Find each white blood cell.
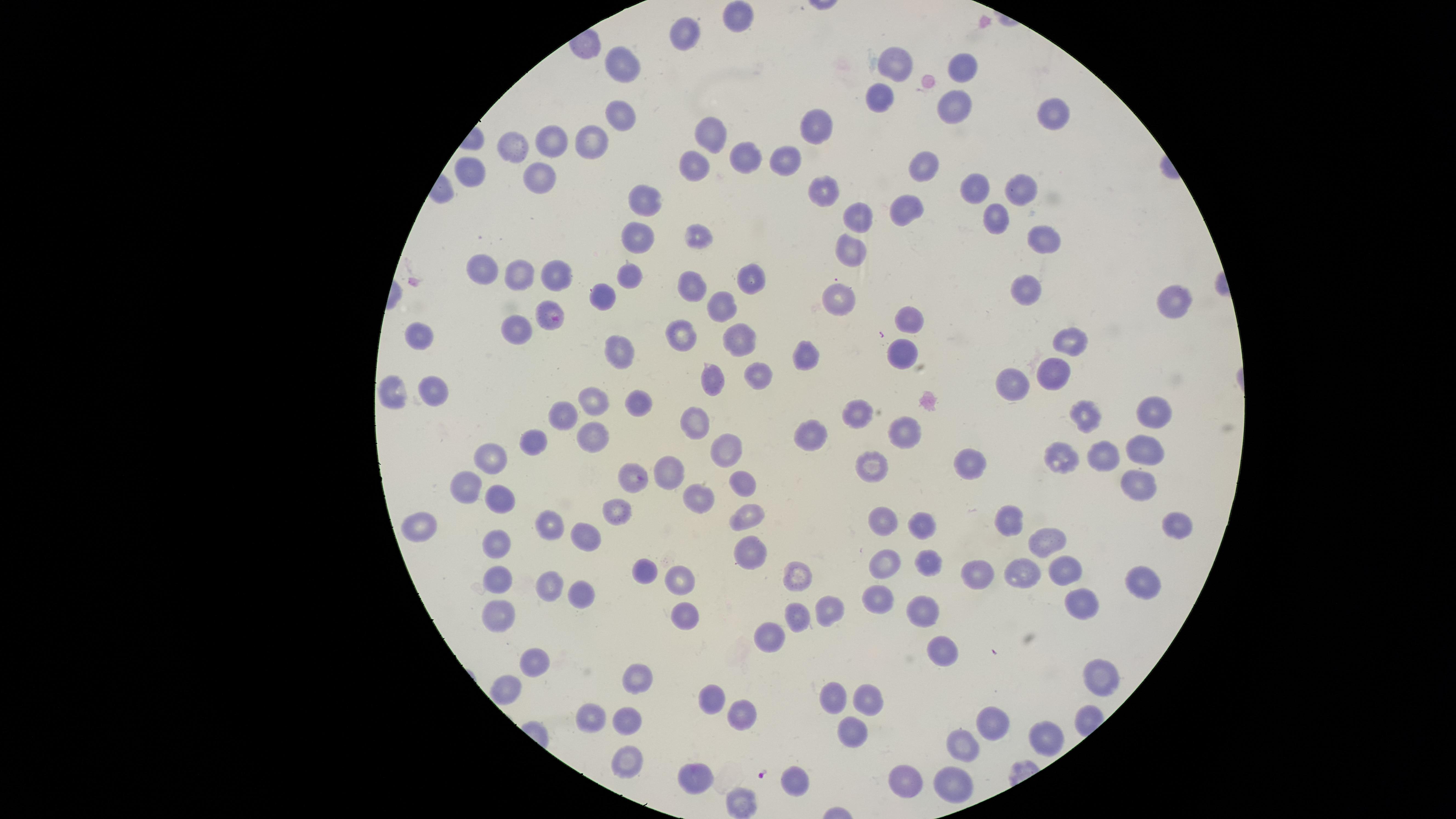

No white blood cells identified.

uninfected red blood cells = approximate marker points, in pixels from the top-left corner: (x=734, y=16), (x=688, y=31), (x=895, y=62), (x=622, y=63), (x=964, y=65), (x=880, y=95), (x=956, y=104), (x=1057, y=109), (x=620, y=119), (x=820, y=122), (x=709, y=127), (x=552, y=137), (x=591, y=139), (x=514, y=144), (x=743, y=158), (x=787, y=158), (x=924, y=165), (x=696, y=167), (x=540, y=174), (x=472, y=176), (x=1018, y=186), (x=820, y=187), (x=973, y=189), (x=644, y=201), (x=905, y=209), (x=858, y=212), (x=994, y=215), (x=696, y=233), (x=1039, y=233), (x=636, y=239), (x=850, y=245), (x=484, y=269), (x=517, y=272), (x=555, y=275), (x=628, y=275), (x=751, y=279), (x=691, y=288), (x=1025, y=290), (x=603, y=297), (x=840, y=299), (x=1179, y=300), (x=722, y=303), (x=910, y=317), (x=514, y=330), (x=680, y=333), (x=420, y=337), (x=1071, y=337), (x=737, y=339), (x=619, y=351), (x=904, y=351), (x=809, y=354), (x=1051, y=371), (x=757, y=372), (x=715, y=379), (x=1011, y=384), (x=395, y=389), (x=435, y=391), (x=635, y=399), (x=591, y=401), (x=1153, y=410), (x=863, y=412), (x=1081, y=412), (x=566, y=413), (x=695, y=423), (x=816, y=430), (x=910, y=431), (x=595, y=433), (x=727, y=443), (x=1144, y=443), (x=532, y=444), (x=1103, y=454), (x=496, y=455), (x=1063, y=457), (x=969, y=461), (x=874, y=464), (x=670, y=465), (x=628, y=476), (x=744, y=482), (x=1140, y=482), (x=474, y=486), (x=702, y=495), (x=501, y=498), (x=614, y=512), (x=750, y=512), (x=1007, y=519), (x=881, y=522), (x=1176, y=523), (x=418, y=525), (x=550, y=527), (x=924, y=527), (x=589, y=534), (x=1049, y=537), (x=497, y=542), (x=749, y=549), (x=927, y=562), (x=886, y=567), (x=1064, y=570), (x=651, y=571), (x=794, y=573), (x=977, y=574), (x=1019, y=574), (x=1145, y=579), (x=682, y=580), (x=496, y=581), (x=547, y=582), (x=582, y=593), (x=881, y=598), (x=1080, y=604), (x=682, y=606), (x=830, y=606), (x=925, y=610), (x=802, y=613), (x=496, y=616), (x=771, y=641), (x=939, y=650), (x=535, y=661), (x=637, y=676), (x=1101, y=677), (x=505, y=691), (x=867, y=695), (x=835, y=696), (x=714, y=700), (x=741, y=712), (x=598, y=714), (x=626, y=716), (x=994, y=725), (x=852, y=727), (x=1045, y=737), (x=963, y=743), (x=621, y=756), (x=695, y=773), (x=794, y=777), (x=904, y=781), (x=948, y=782), (x=741, y=802)
preparation = thin smear of blood
image size = 1456×819 pixels
presence = malaria parasites seen
visible region = circular
capture = smartphone photograph through the microscope eyepiece
field of view = single
stain = Giemsa
parasitized red blood cells = approximate marker points, in pixels from the top-left corner: (x=552, y=319)
species = Plasmodium falciparum